Identify the blood parasite species.
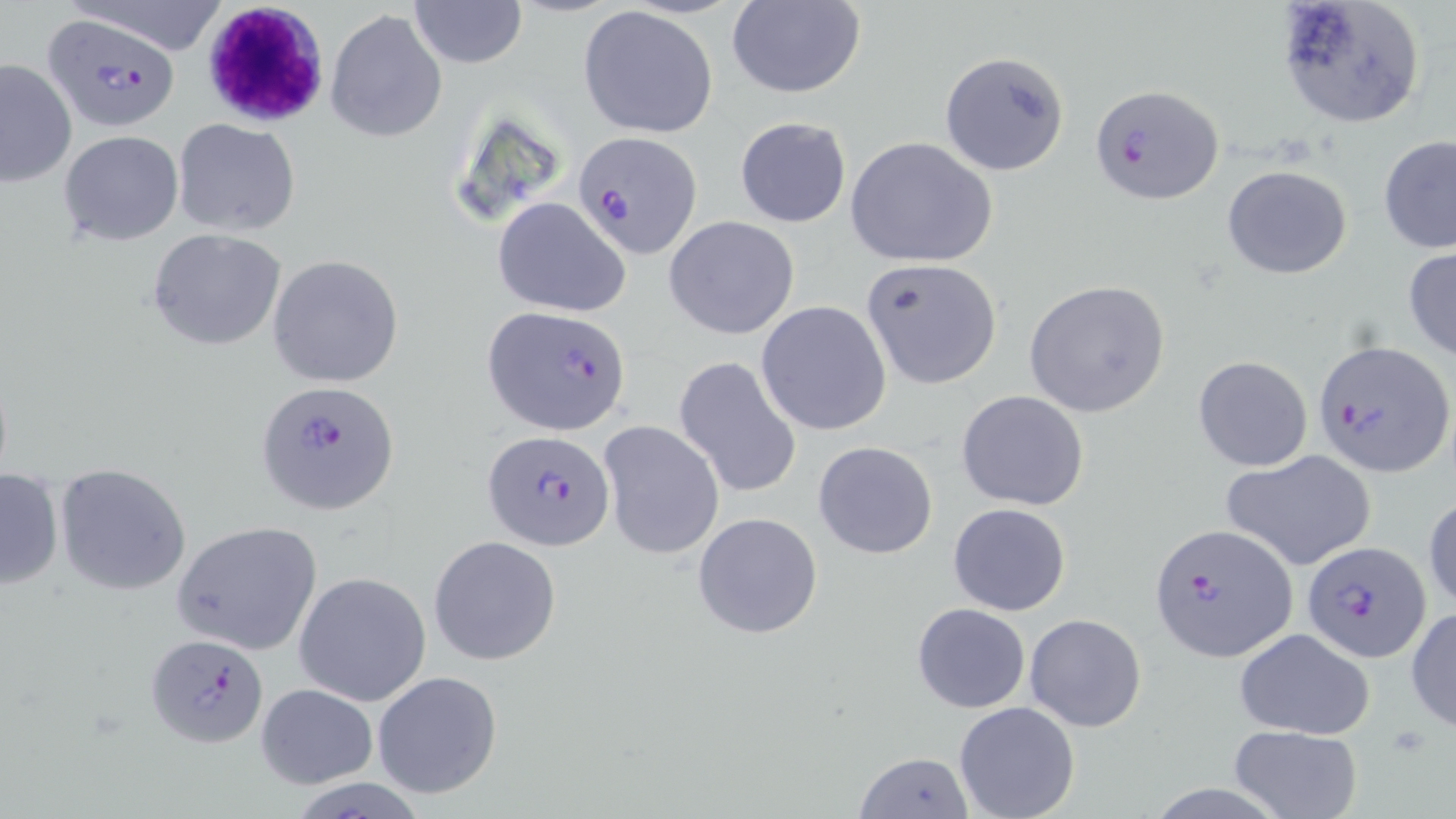
Plasmodium falciparum.

Approximate bounding boxes as (x1, y1, x2, y2) in pixels. White blood cell locations: (200, 1, 332, 129). Plasmodium falciparum-infected red blood cell locations: (44, 15, 182, 132), (1090, 83, 1223, 205), (572, 132, 704, 259), (486, 308, 630, 432), (1311, 338, 1454, 475), (255, 380, 400, 516), (483, 429, 615, 551), (1148, 523, 1297, 660), (1303, 540, 1432, 663), (145, 632, 267, 746). Uninfected red blood cell locations: (411, 0, 526, 68), (726, 0, 866, 98), (1275, 0, 1428, 128), (577, 5, 720, 139), (326, 8, 447, 142), (941, 52, 1070, 176), (0, 57, 76, 189), (735, 116, 851, 229), (173, 119, 302, 237), (58, 130, 183, 246), (845, 136, 997, 268), (1379, 136, 1456, 255), (701, 162, 827, 325), (1222, 165, 1352, 279), (492, 196, 632, 317), (663, 215, 800, 340), (146, 228, 290, 352), (1404, 247, 1456, 362), (267, 254, 405, 389), (860, 258, 1003, 389), (1023, 280, 1172, 417), (757, 301, 893, 436), (1193, 355, 1313, 471), (674, 356, 802, 499), (956, 390, 1091, 511), (598, 419, 725, 561), (813, 440, 938, 560), (1222, 450, 1376, 571), (55, 463, 192, 596), (0, 466, 65, 593), (1423, 491, 1456, 613), (948, 501, 1072, 616), (693, 511, 824, 639), (171, 521, 322, 654), (429, 535, 562, 667), (294, 571, 432, 707), (911, 603, 1031, 713), (1407, 606, 1456, 732), (1024, 612, 1147, 733), (1233, 628, 1375, 742), (372, 671, 504, 799), (254, 684, 378, 788), (954, 700, 1081, 819), (1228, 725, 1362, 819), (851, 752, 974, 818). Thin blood film. Light microscopy. 1000x magnification. Image is 1456×819 pixels. May-Grünwald-Giemsa stain. Single field of view.